Point out each malaria parasite.
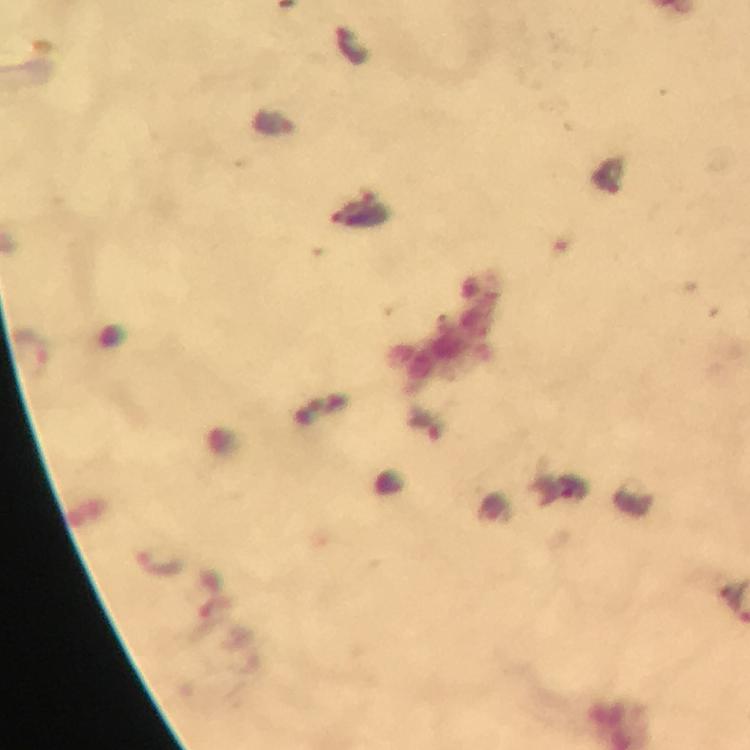
Approximate centers as [x, y] in pixels.
Malaria parasites: [157, 560].

Summary:
  - Preparation: thick blood smear
  - Stain: Giemsa
  - Capture: smartphone camera through the microscope
  - Cropped from: one field of view
  - Context: from a malaria diagnostic workup
  - Immersion oil: applied
  - Magnification: 100x
  - Image size: 750×750 pixels